Name the cell type shown.
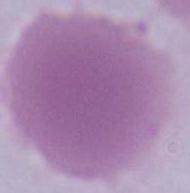
An erythrocyte.

1000x magnification. Micrograph.